Assess the morphology of the erythrocytes.
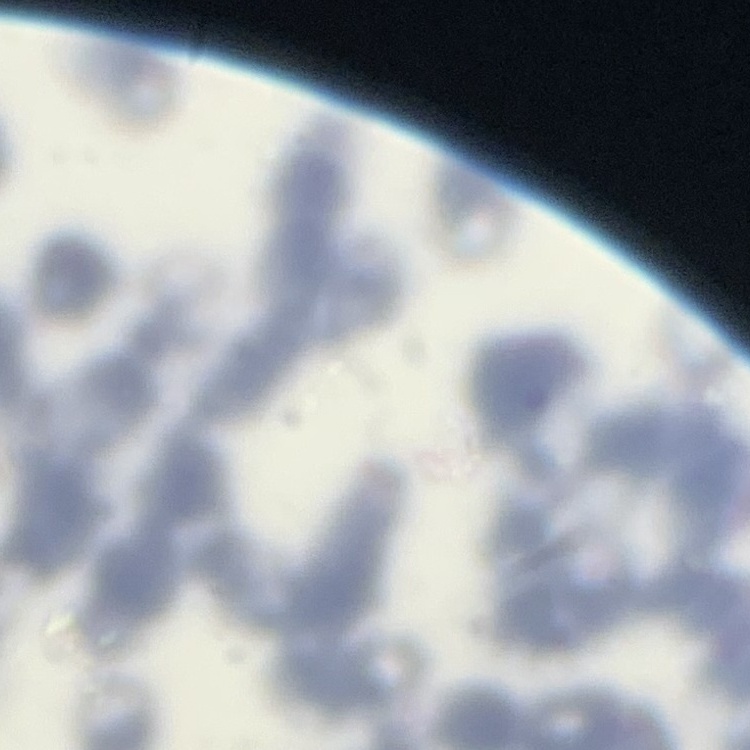
They show rouleaux formation.

{
  "image_type": "square crop of a larger photomicrograph",
  "preparation": "thin blood smear",
  "stain": "Field's or Giemsa"
}